Classify this cell by malaria status.
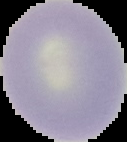
It is uninfected.

From a thin blood film. Image is 127×142 pixels. Segmented cell region on a black background.